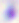

Toxoplasma gondii is shown. Photomicrograph. Captured at 400x magnification.